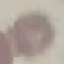
Malaria status: uninfected. Giemsa-stained preparation. Thin blood smear. Photographed with a smartphone camera at the microscope eyepiece. Cell patch, automatically extracted from a larger field of view and resized to 64 × 64 pixels.